Give the preparation type.
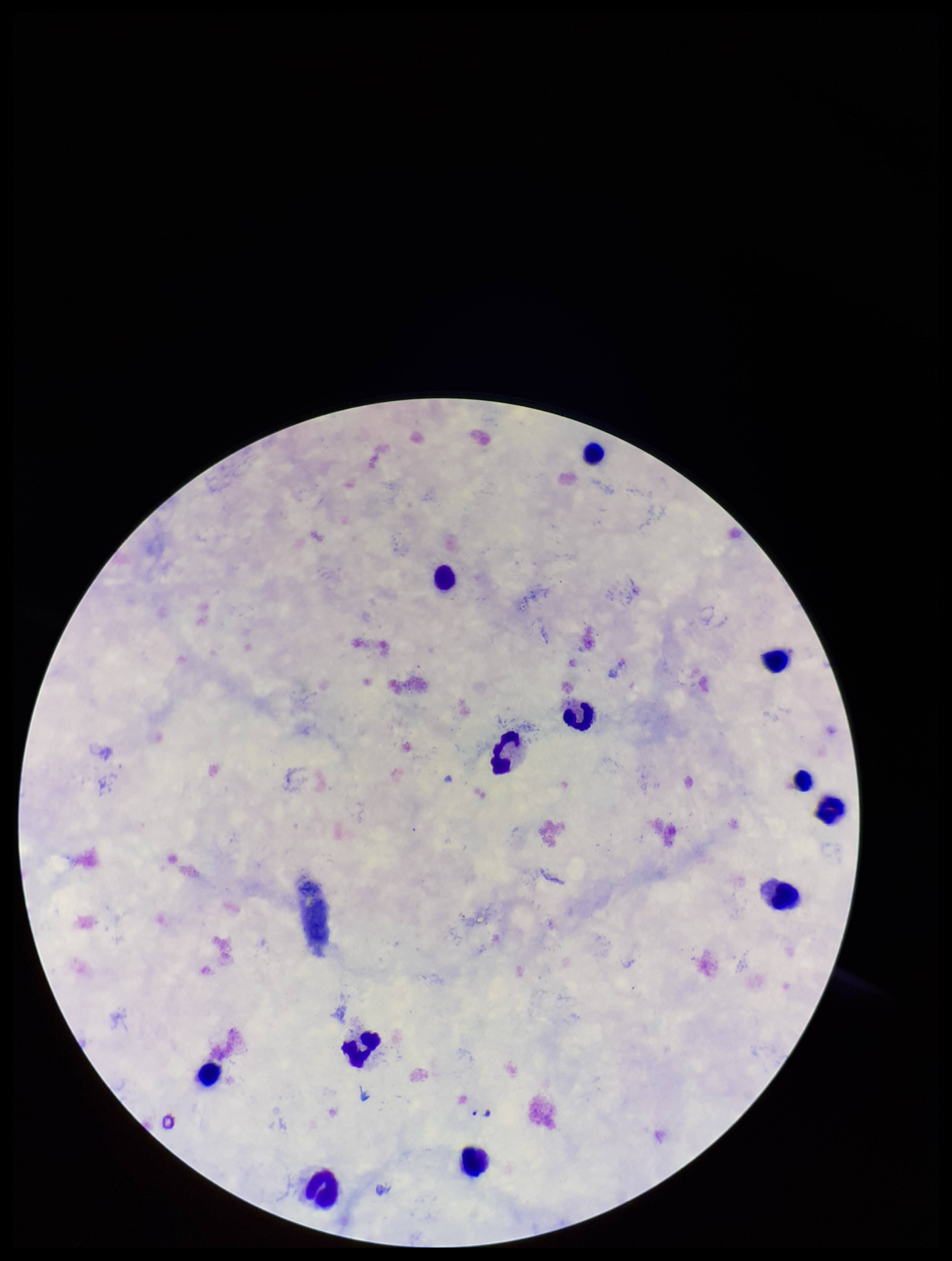
Thick.

field of view = single
Plasmodium parasites = none identified
image size = 952×1261 pixels
patient malaria status = positive
species reported for this patient = Plasmodium falciparum
capture = smartphone photograph through the microscope eyepiece
leukocyte count = 12
parasite count = 0
stain = Giemsa